Name the blood parasite species.
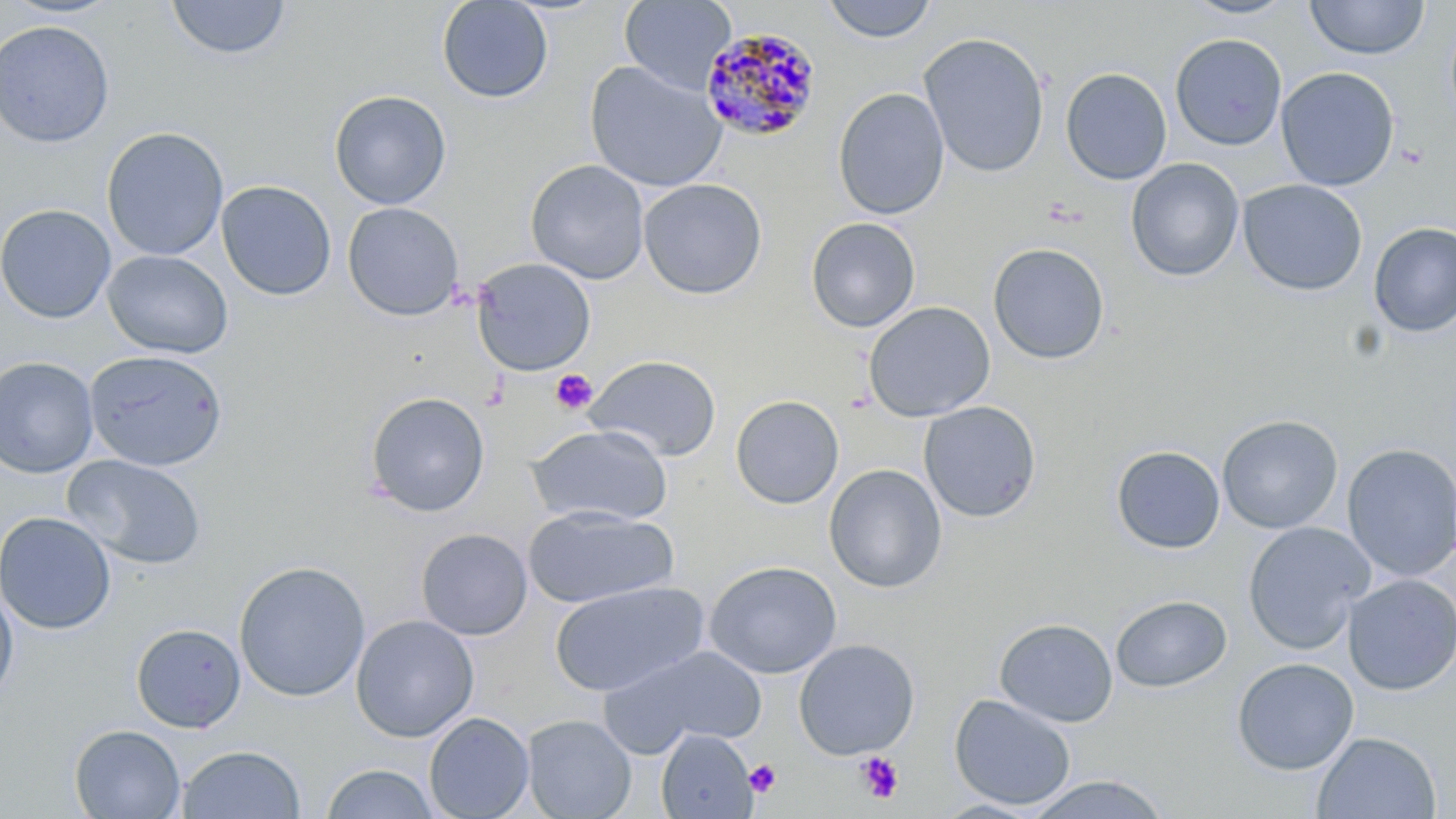
Plasmodium malariae.

Approximate bounding boxes as (x1, y1, x2, y2) in pixels. Uninfected red blood cell locations: (1, 0, 124, 20), (166, 0, 292, 61), (436, 0, 554, 103), (619, 0, 737, 94), (821, 0, 937, 43), (1182, 0, 1300, 20), (1305, 0, 1430, 60), (0, 20, 115, 148), (918, 32, 1051, 178), (1170, 33, 1287, 151), (584, 60, 727, 193), (1275, 66, 1400, 191), (1060, 67, 1172, 185), (833, 88, 950, 220), (329, 90, 452, 210), (101, 127, 229, 261), (1125, 158, 1245, 282), (525, 159, 650, 285), (638, 178, 767, 299), (1237, 179, 1368, 297), (216, 180, 337, 300), (342, 202, 465, 321), (0, 204, 116, 323), (805, 217, 921, 333), (1368, 222, 1456, 337), (988, 242, 1110, 364), (102, 249, 233, 359), (471, 257, 596, 376), (863, 301, 996, 422), (84, 350, 229, 471), (585, 355, 722, 462), (0, 356, 99, 478), (364, 391, 490, 518), (730, 394, 844, 509), (919, 401, 1041, 522), (1216, 414, 1343, 534), (526, 424, 673, 528), (1341, 443, 1455, 582), (1112, 445, 1226, 554), (63, 454, 207, 570), (823, 464, 948, 593), (523, 506, 678, 609), (0, 511, 117, 635), (1241, 521, 1376, 655), (415, 528, 533, 641), (233, 560, 372, 702), (703, 560, 842, 679), (1342, 574, 1456, 696), (549, 581, 709, 697), (0, 584, 19, 700), (1110, 594, 1232, 692), (350, 614, 479, 742), (994, 618, 1118, 728), (130, 622, 246, 733), (793, 639, 920, 760), (602, 645, 769, 756), (1231, 657, 1359, 775), (949, 694, 1077, 811), (424, 712, 534, 819), (522, 714, 636, 819), (69, 724, 186, 818), (656, 729, 757, 819), (1312, 731, 1441, 818), (176, 744, 306, 819), (321, 763, 440, 819), (1024, 774, 1172, 818). Platelet locations: (1396, 143, 1429, 169), (550, 368, 598, 415), (855, 751, 904, 804), (745, 758, 782, 797). Plasmodium malariae-infected red blood cell locations: (699, 26, 822, 143). Image is 1456×819 pixels. May-Grünwald-Giemsa-stained preparation. One field of a larger specimen. 1000x magnification. Thin blood smear. Light microscopy.